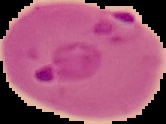

Summary:
  - Malaria status: parasitized
  - Preparation: thin blood smear
  - Image size: 166×124 pixels
  - Image type: cell region segmented out of the field of view; surrounding area masked to black